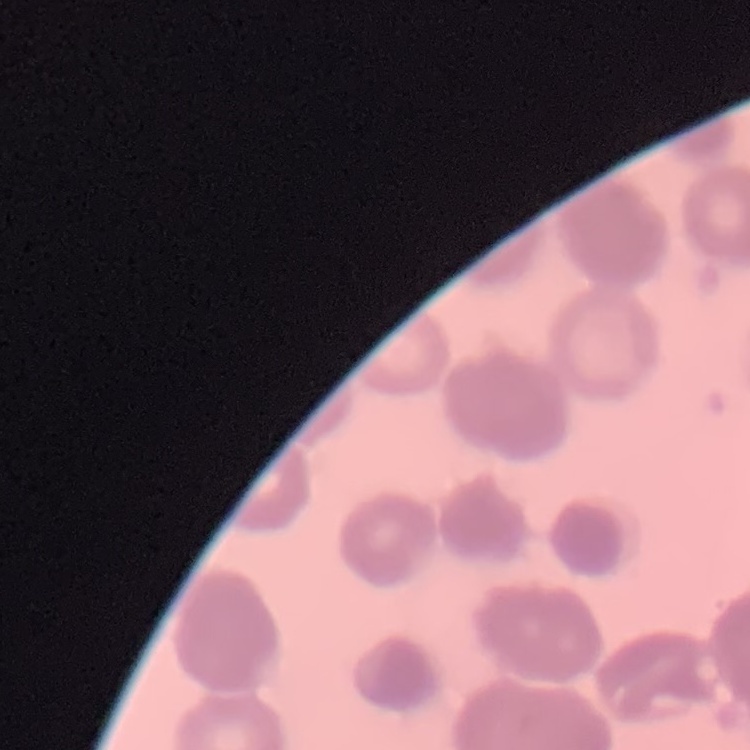

{
  "red_blood_cell_morphology": "rouleaux formation",
  "stain": "Field's or Giemsa",
  "preparation": "thin blood smear",
  "image_type": "one tile cut from a larger photomicrograph"
}